Outline each white blood cell.
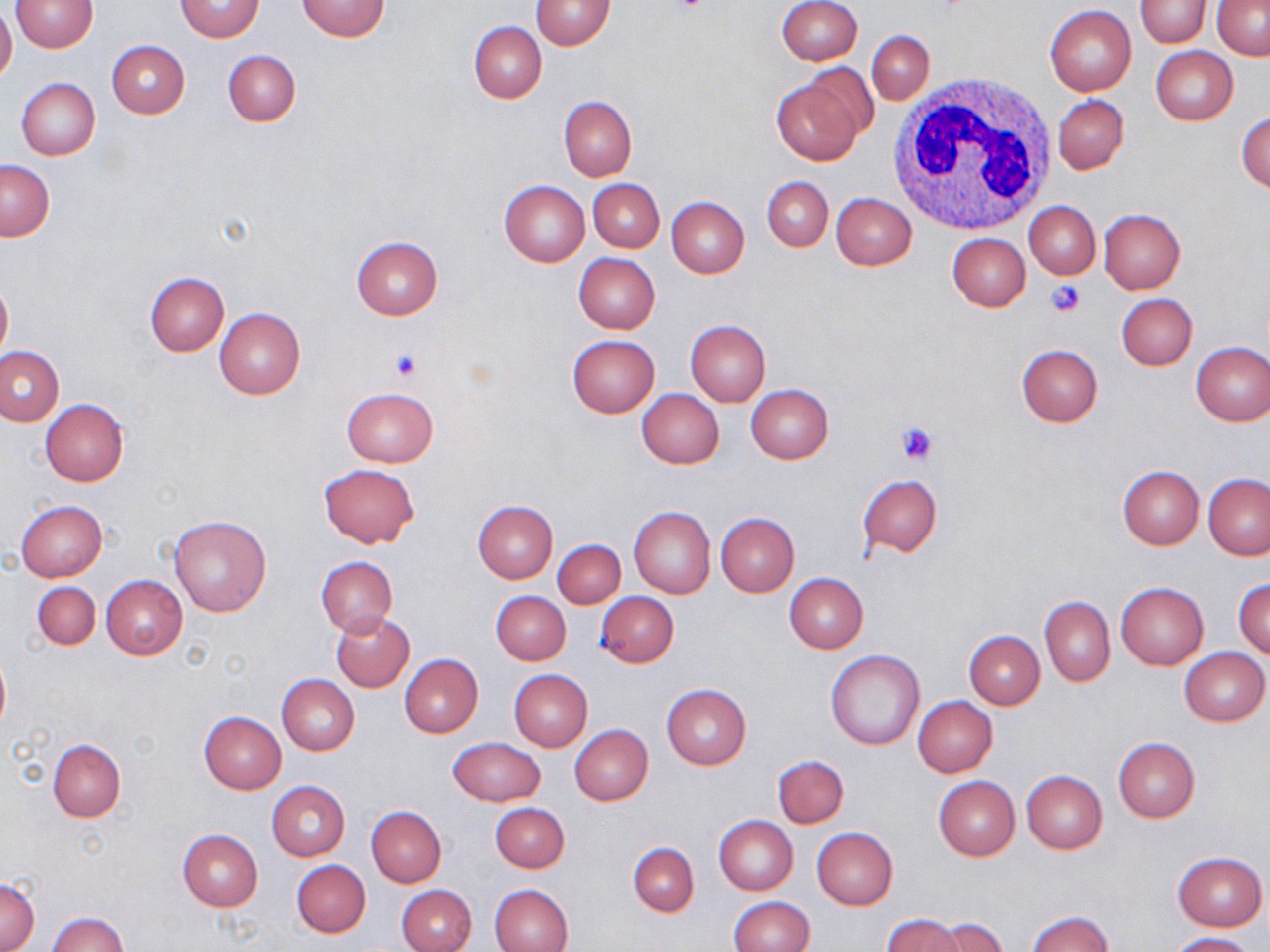

Approximate bounding boxes as named x1/y1/x2/y2 corners in pixels.
White blood cells: (x1=889, y1=71, x2=1063, y2=235).

Uninfected red blood cell locations: (x1=10, y1=0, x2=98, y2=51), (x1=296, y1=0, x2=391, y2=42), (x1=531, y1=0, x2=615, y2=50), (x1=1135, y1=0, x2=1210, y2=47), (x1=1212, y1=0, x2=1270, y2=59), (x1=175, y1=1, x2=263, y2=41), (x1=775, y1=1, x2=862, y2=66), (x1=0, y1=5, x2=17, y2=85), (x1=1044, y1=6, x2=1137, y2=96), (x1=468, y1=21, x2=546, y2=103), (x1=867, y1=31, x2=934, y2=103), (x1=106, y1=40, x2=189, y2=119), (x1=1151, y1=46, x2=1237, y2=124), (x1=222, y1=49, x2=300, y2=127), (x1=770, y1=73, x2=870, y2=166), (x1=15, y1=78, x2=100, y2=159), (x1=1052, y1=94, x2=1129, y2=174), (x1=559, y1=96, x2=636, y2=181), (x1=1236, y1=111, x2=1270, y2=193), (x1=1, y1=159, x2=53, y2=240), (x1=762, y1=176, x2=833, y2=251), (x1=588, y1=179, x2=664, y2=252), (x1=498, y1=180, x2=589, y2=267), (x1=831, y1=193, x2=917, y2=270), (x1=666, y1=197, x2=749, y2=278), (x1=1024, y1=201, x2=1100, y2=279), (x1=1097, y1=209, x2=1184, y2=294), (x1=947, y1=233, x2=1030, y2=311), (x1=350, y1=236, x2=443, y2=320), (x1=573, y1=253, x2=660, y2=334), (x1=144, y1=272, x2=228, y2=356), (x1=0, y1=277, x2=12, y2=361), (x1=1116, y1=293, x2=1198, y2=370), (x1=214, y1=307, x2=305, y2=399), (x1=684, y1=319, x2=771, y2=405), (x1=567, y1=335, x2=659, y2=417), (x1=1190, y1=342, x2=1270, y2=425), (x1=1016, y1=344, x2=1103, y2=426), (x1=0, y1=345, x2=66, y2=426), (x1=746, y1=384, x2=833, y2=463), (x1=341, y1=387, x2=439, y2=467), (x1=637, y1=388, x2=725, y2=469), (x1=41, y1=400, x2=129, y2=486), (x1=318, y1=464, x2=419, y2=548), (x1=1118, y1=465, x2=1204, y2=549), (x1=857, y1=474, x2=942, y2=556), (x1=1203, y1=474, x2=1269, y2=560), (x1=472, y1=500, x2=557, y2=582), (x1=15, y1=501, x2=107, y2=580), (x1=628, y1=505, x2=715, y2=598), (x1=716, y1=512, x2=799, y2=596), (x1=168, y1=517, x2=271, y2=617), (x1=552, y1=538, x2=626, y2=608), (x1=315, y1=556, x2=397, y2=639), (x1=784, y1=573, x2=868, y2=652), (x1=101, y1=575, x2=187, y2=659), (x1=1233, y1=578, x2=1270, y2=659), (x1=32, y1=581, x2=100, y2=650), (x1=1115, y1=583, x2=1208, y2=669), (x1=491, y1=592, x2=570, y2=665), (x1=596, y1=592, x2=678, y2=667), (x1=1039, y1=596, x2=1114, y2=686), (x1=330, y1=611, x2=414, y2=693), (x1=964, y1=630, x2=1044, y2=708), (x1=0, y1=647, x2=10, y2=740), (x1=1179, y1=648, x2=1268, y2=726), (x1=826, y1=649, x2=925, y2=749), (x1=399, y1=653, x2=483, y2=737), (x1=509, y1=669, x2=593, y2=751), (x1=277, y1=674, x2=359, y2=755), (x1=661, y1=683, x2=751, y2=769), (x1=913, y1=696, x2=997, y2=777), (x1=199, y1=712, x2=286, y2=793), (x1=569, y1=724, x2=653, y2=805), (x1=449, y1=737, x2=545, y2=807), (x1=1113, y1=737, x2=1200, y2=822), (x1=49, y1=740, x2=124, y2=821), (x1=773, y1=755, x2=849, y2=826), (x1=1021, y1=770, x2=1107, y2=853), (x1=932, y1=776, x2=1020, y2=860), (x1=266, y1=780, x2=350, y2=860), (x1=490, y1=803, x2=569, y2=872), (x1=366, y1=806, x2=445, y2=887), (x1=714, y1=815, x2=798, y2=895), (x1=810, y1=827, x2=898, y2=911), (x1=178, y1=829, x2=262, y2=911), (x1=627, y1=843, x2=698, y2=915), (x1=1172, y1=852, x2=1266, y2=931), (x1=290, y1=860, x2=370, y2=938), (x1=0, y1=879, x2=39, y2=950), (x1=487, y1=883, x2=572, y2=952), (x1=396, y1=884, x2=476, y2=952), (x1=728, y1=897, x2=814, y2=952), (x1=1026, y1=910, x2=1113, y2=952), (x1=47, y1=912, x2=128, y2=952), (x1=881, y1=914, x2=965, y2=952), (x1=933, y1=917, x2=1008, y2=952), (x1=1167, y1=931, x2=1257, y2=952). Platelet locations: (x1=670, y1=0, x2=709, y2=18), (x1=1044, y1=280, x2=1085, y2=318), (x1=391, y1=349, x2=422, y2=382), (x1=896, y1=420, x2=939, y2=463). Slide-level diagnosis: negative for blood parasites. Thin blood film. May-Grünwald-Giemsa stain. 1000x magnification. One field of a larger specimen. Image is 1270×952 pixels. Optical microscopy.